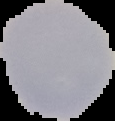

image type = cell region segmented out of the field of view; surrounding area masked to black
malaria status = uninfected
preparation = thin blood smear
image size = 115×121 pixels